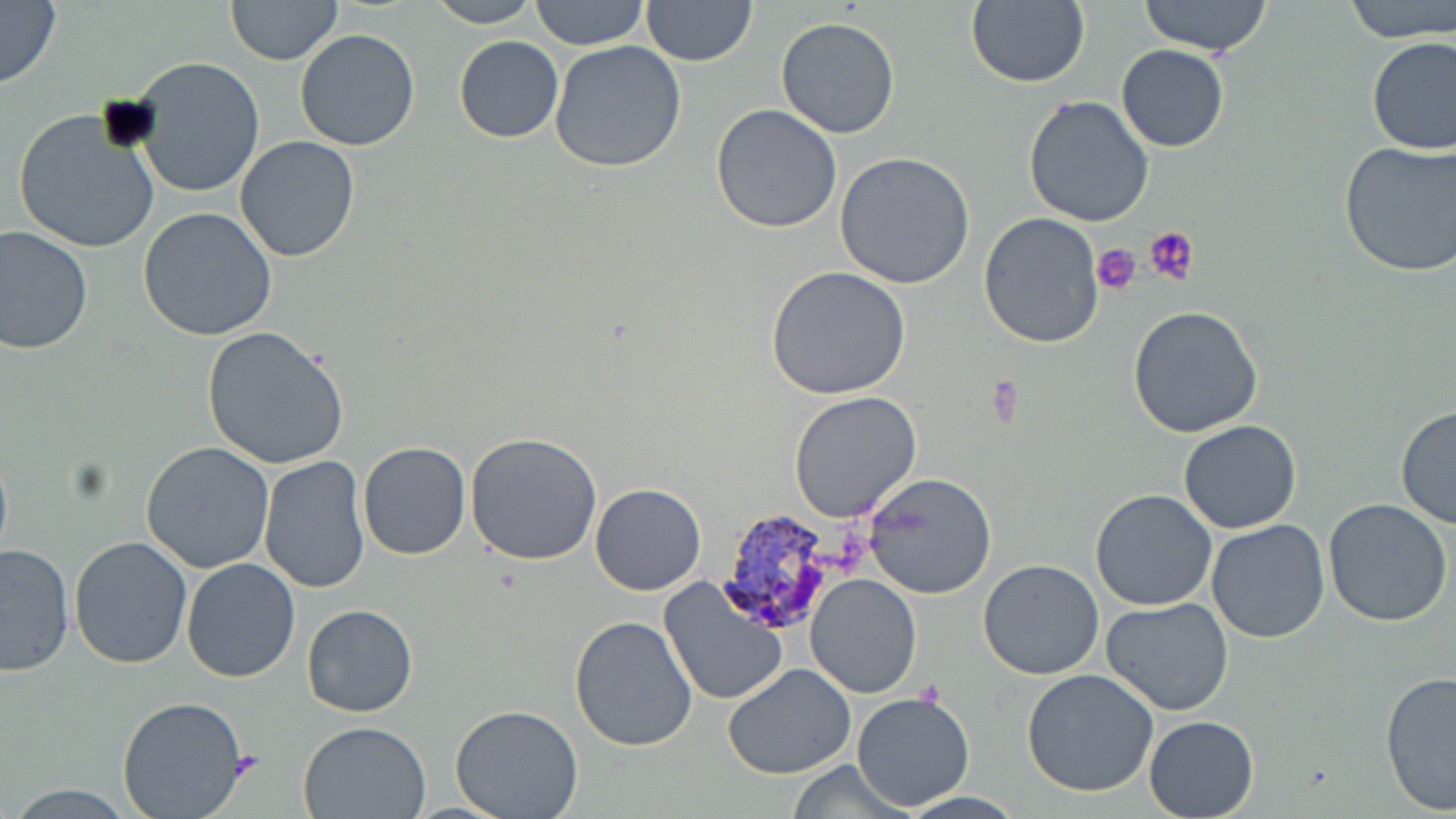

Summary:
  - Coordinate format: approximate bounding boxes as [x1, y1, x2, y2] in pixels
  - Plasmodium vivax-infected red blood cell locations: [719, 507, 849, 633]
  - Platelet locations: [1143, 225, 1197, 287], [1092, 243, 1141, 295], [231, 751, 263, 781]
  - Uninfected red blood cell locations: [226, 0, 343, 66], [530, 0, 648, 50], [640, 0, 758, 67], [966, 0, 1091, 88], [1139, 0, 1275, 57], [1342, 0, 1456, 44], [0, 1, 62, 92], [423, 1, 543, 27], [775, 17, 902, 139], [295, 29, 421, 151], [454, 36, 564, 143], [1365, 36, 1455, 156], [550, 41, 686, 174], [1114, 44, 1230, 153], [130, 56, 266, 198], [1022, 95, 1154, 228], [711, 104, 841, 232], [12, 108, 159, 252], [234, 136, 361, 262], [1340, 137, 1454, 276], [834, 153, 975, 289], [138, 207, 277, 341], [977, 213, 1105, 349], [0, 225, 95, 354], [766, 266, 913, 400], [1128, 304, 1264, 438], [203, 326, 350, 468], [790, 391, 922, 522], [1395, 404, 1456, 531], [1178, 421, 1302, 535], [465, 431, 602, 565], [141, 441, 275, 574], [356, 442, 471, 561], [259, 455, 371, 594], [864, 473, 996, 600], [590, 483, 706, 595], [1090, 489, 1217, 611], [1322, 498, 1455, 627], [1206, 518, 1330, 645], [69, 536, 194, 669], [0, 542, 75, 676], [181, 558, 302, 682], [978, 558, 1106, 680], [807, 575, 923, 700], [657, 578, 789, 707], [1102, 597, 1235, 717], [301, 603, 418, 717], [570, 615, 698, 754], [723, 664, 856, 780], [1022, 669, 1159, 797], [1380, 671, 1456, 814], [850, 690, 976, 812], [116, 696, 250, 818], [450, 706, 584, 819], [1142, 715, 1258, 818], [298, 721, 431, 819], [784, 760, 914, 818]
  - Slide-level diagnosis: Plasmodium vivax
  - Modality: optical microscopy
  - Preparation: thin blood smear
  - Magnification: 1000x
  - Field of view: single
  - Image size: 1456×819 pixels
  - Stain: May-Grünwald-Giemsa